Classify this cell by malaria status.
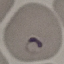

It is parasitized.

Giemsa stain. Cell patch, automatically extracted from a larger field of view and resized to 64 × 64 pixels. Thin smear of blood. Photographed with a smartphone camera at the microscope eyepiece.